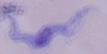
Summary:
  - Modality: micrograph
  - Identification: trypanosome
  - Magnification: 1000x